Comment on the morphology of the red blood cells.
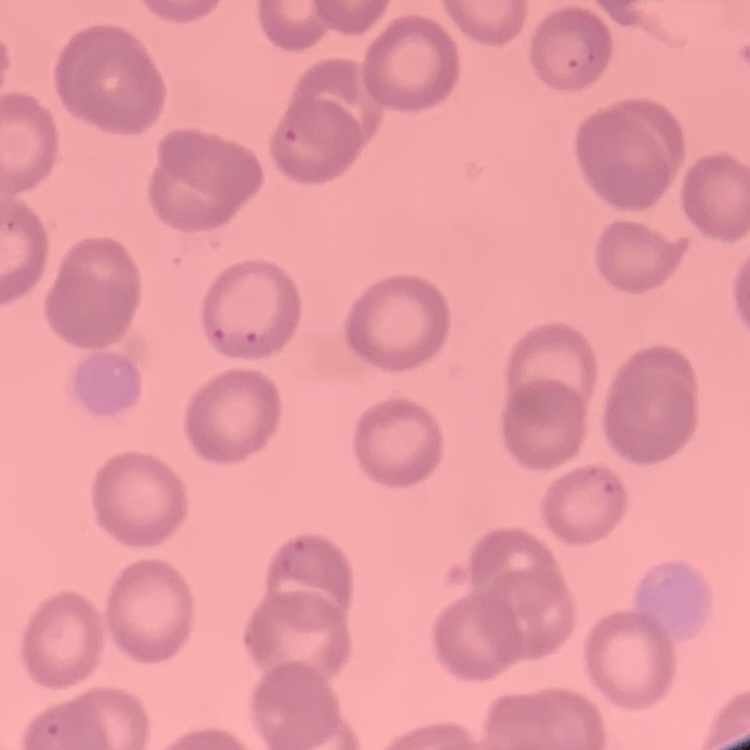
They show no rouleaux formation.

Thin blood film. Square crop of a larger photomicrograph. Field's or Giemsa stain.